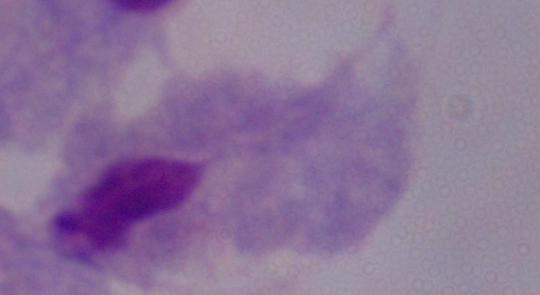
identification = trichomonad
modality = micrograph
magnification = 1000x